Assess this cell for malaria.
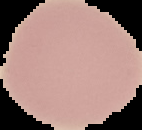
It is uninfected.

Segmented cell region on a black background. Image is 142×130 pixels. From a thin blood film.